Locate and identify every blood parasite.
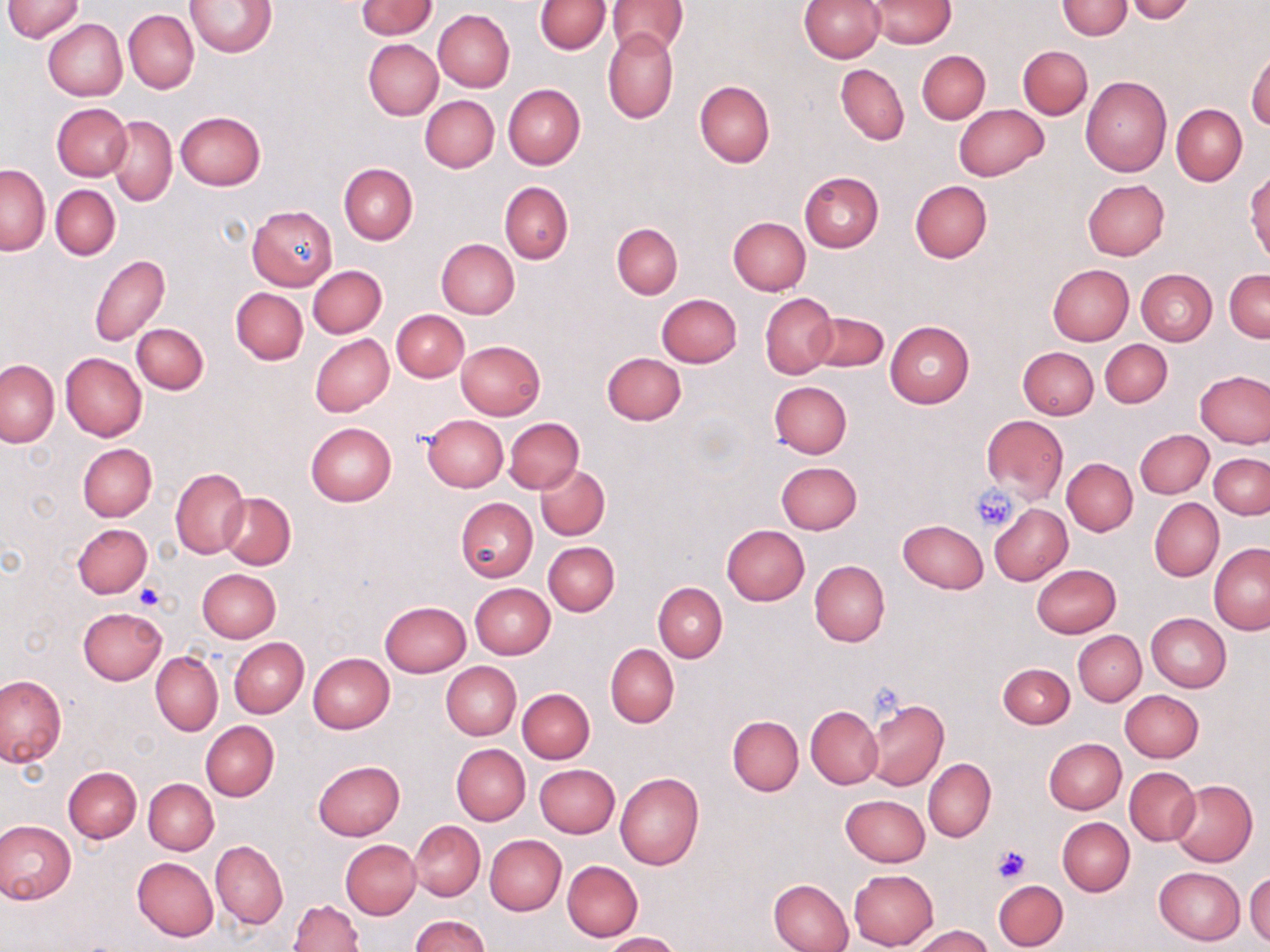

No blood parasites observed.

slide-level diagnosis = negative for blood parasites
stain = May-Grünwald-Giemsa
modality = optical microscopy
image size = 1270×952 pixels
preparation = thin blood smear
field of view = one of a larger specimen
magnification = 1000x
platelet locations = approximate bounding boxes as [x1, y1, x2, y2] in pixels: [970, 486, 1020, 531], [133, 584, 165, 612], [990, 842, 1033, 884]
uninfected red blood cell locations = approximate bounding boxes as [x1, y1, x2, y2] in pixels: [3, 0, 85, 42], [358, 0, 436, 39], [535, 0, 609, 54], [608, 0, 687, 57], [801, 0, 884, 62], [866, 0, 957, 48], [1057, 0, 1131, 40], [187, 1, 276, 56], [1123, 1, 1197, 23], [118, 5, 268, 76], [124, 9, 199, 93], [433, 10, 514, 92], [42, 18, 127, 101], [603, 27, 678, 124], [363, 39, 443, 121], [1018, 45, 1091, 119], [1246, 47, 1270, 131], [917, 50, 990, 123], [836, 64, 909, 145], [1080, 76, 1171, 176], [694, 80, 774, 166], [503, 83, 585, 168], [420, 95, 499, 172], [52, 103, 130, 180], [954, 104, 1049, 181], [1172, 104, 1247, 185], [174, 112, 266, 191], [106, 115, 177, 205], [338, 163, 417, 244], [1, 165, 51, 255], [1246, 170, 1270, 264], [798, 172, 884, 252], [1083, 179, 1170, 260], [499, 181, 573, 264], [909, 181, 992, 261], [51, 185, 120, 260], [247, 206, 336, 289], [728, 217, 809, 296], [611, 223, 682, 298], [436, 239, 520, 318], [90, 255, 170, 346], [308, 265, 386, 338], [1047, 265, 1134, 346], [1136, 269, 1217, 345], [1225, 269, 1270, 343], [231, 288, 307, 365], [657, 293, 741, 367], [761, 293, 837, 379], [392, 310, 469, 381], [807, 312, 889, 371], [885, 321, 975, 409], [132, 322, 209, 394], [311, 334, 393, 416], [1100, 339, 1172, 408], [456, 340, 546, 419], [1018, 346, 1098, 419], [60, 352, 146, 442], [602, 352, 686, 424], [0, 360, 59, 448], [1195, 370, 1269, 448], [770, 381, 853, 459], [421, 414, 507, 492], [520, 415, 600, 542], [980, 416, 1069, 503], [505, 418, 583, 492], [305, 423, 396, 506], [1134, 430, 1213, 499], [77, 442, 157, 522], [1209, 453, 1270, 518], [1062, 459, 1138, 535], [775, 461, 862, 534], [536, 464, 609, 540], [171, 467, 249, 559], [219, 493, 295, 568], [456, 498, 537, 581], [1149, 499, 1223, 580], [989, 504, 1073, 585], [897, 520, 987, 594], [73, 523, 152, 599], [721, 525, 809, 605], [543, 541, 620, 616], [1209, 544, 1270, 635], [809, 560, 889, 648], [1031, 564, 1121, 638], [197, 568, 281, 642], [470, 583, 555, 659], [654, 583, 727, 662], [380, 600, 471, 676], [78, 607, 166, 684], [1146, 613, 1231, 692], [1073, 631, 1145, 706], [230, 638, 309, 718], [606, 644, 679, 727], [150, 652, 223, 735], [308, 653, 395, 734], [441, 662, 520, 740], [998, 663, 1074, 728], [0, 674, 68, 767], [518, 688, 595, 763], [1121, 690, 1203, 761], [867, 700, 948, 790], [806, 706, 883, 789], [727, 716, 804, 795], [201, 721, 279, 800], [1044, 737, 1126, 814], [451, 744, 530, 825], [923, 757, 996, 843], [313, 760, 405, 840], [534, 763, 619, 837], [63, 766, 142, 843], [1124, 766, 1200, 846], [1131, 768, 1213, 910], [614, 772, 703, 871], [143, 778, 219, 855], [1170, 779, 1257, 866], [840, 794, 930, 867], [1058, 817, 1135, 895], [0, 819, 76, 903], [410, 820, 485, 901], [485, 834, 566, 915], [340, 840, 420, 919], [211, 841, 287, 928], [132, 857, 219, 941], [562, 860, 643, 942], [1154, 867, 1246, 946], [849, 869, 938, 950], [1246, 871, 1270, 945], [769, 878, 855, 952], [993, 879, 1067, 949], [288, 899, 363, 951], [409, 915, 489, 952], [911, 925, 994, 952], [602, 932, 680, 952]